Name the cell type shown.
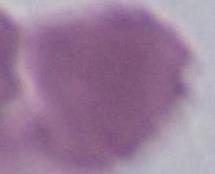

This is an erythrocyte.

Summary:
  - Modality: photomicrograph
  - Magnification: 1000x